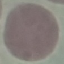
Summary:
  - Result: negative for malaria parasites
  - Preparation: thin smear
  - Stain: Giemsa
  - Image type: cell patch, automatically extracted from a larger field of view and resized to 64 × 64 pixels
  - Capture: smartphone through the microscope eyepiece